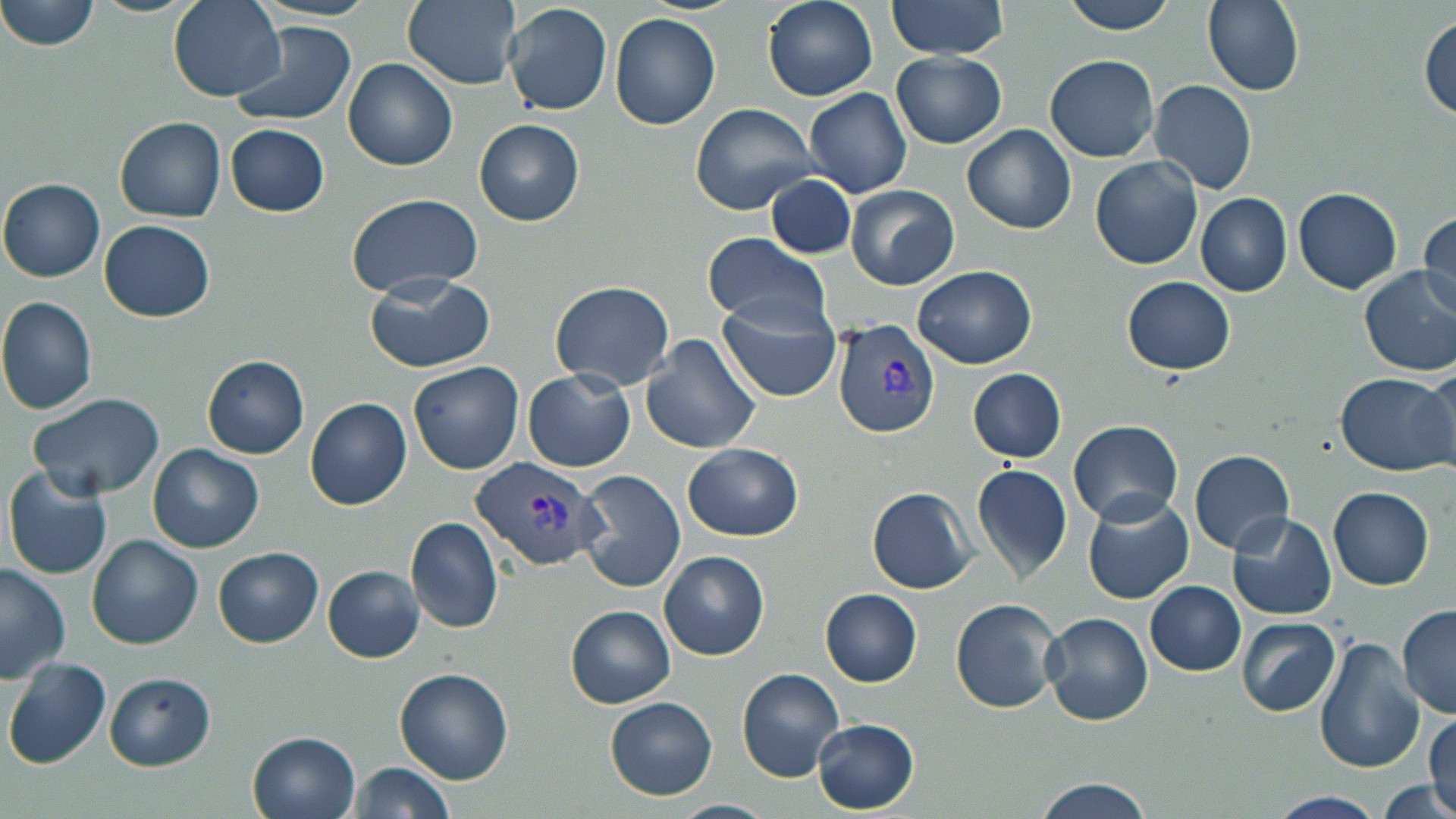

Approximate bounding boxes as named x1/y1/x2/y2 corners in pixels. Plasmodium vivax-infected red blood cell locations: (x1=833, y1=320, x2=939, y2=437), (x1=469, y1=454, x2=606, y2=572). Uninfected red blood cell locations: (x1=3, y1=0, x2=103, y2=50), (x1=169, y1=0, x2=285, y2=100), (x1=403, y1=0, x2=520, y2=89), (x1=763, y1=0, x2=879, y2=101), (x1=885, y1=0, x2=1014, y2=59), (x1=1058, y1=0, x2=1180, y2=34), (x1=1203, y1=0, x2=1304, y2=95), (x1=503, y1=1, x2=612, y2=115), (x1=610, y1=13, x2=722, y2=129), (x1=1419, y1=16, x2=1455, y2=121), (x1=229, y1=22, x2=358, y2=126), (x1=891, y1=51, x2=1008, y2=147), (x1=1045, y1=53, x2=1160, y2=161), (x1=343, y1=58, x2=457, y2=170), (x1=1150, y1=79, x2=1258, y2=195), (x1=805, y1=87, x2=912, y2=199), (x1=691, y1=101, x2=819, y2=215), (x1=115, y1=116, x2=225, y2=222), (x1=475, y1=119, x2=584, y2=225), (x1=226, y1=124, x2=329, y2=216), (x1=962, y1=125, x2=1076, y2=233), (x1=1090, y1=157, x2=1203, y2=269), (x1=766, y1=172, x2=858, y2=260), (x1=1, y1=179, x2=105, y2=281), (x1=844, y1=185, x2=959, y2=290), (x1=1294, y1=186, x2=1402, y2=294), (x1=346, y1=192, x2=482, y2=298), (x1=1195, y1=193, x2=1292, y2=295), (x1=1417, y1=212, x2=1455, y2=316), (x1=98, y1=220, x2=214, y2=322), (x1=702, y1=232, x2=833, y2=332), (x1=913, y1=265, x2=1039, y2=368), (x1=1358, y1=266, x2=1456, y2=376), (x1=364, y1=274, x2=494, y2=372), (x1=1122, y1=276, x2=1236, y2=375), (x1=550, y1=280, x2=675, y2=391), (x1=717, y1=296, x2=843, y2=404), (x1=0, y1=297, x2=97, y2=414), (x1=643, y1=335, x2=762, y2=457), (x1=202, y1=356, x2=310, y2=458), (x1=409, y1=361, x2=524, y2=474), (x1=1422, y1=363, x2=1456, y2=467), (x1=969, y1=368, x2=1067, y2=463), (x1=524, y1=370, x2=635, y2=472), (x1=1337, y1=372, x2=1456, y2=474), (x1=29, y1=393, x2=166, y2=499), (x1=306, y1=398, x2=412, y2=510), (x1=1068, y1=419, x2=1183, y2=526), (x1=682, y1=441, x2=802, y2=540), (x1=150, y1=443, x2=263, y2=553), (x1=1189, y1=448, x2=1294, y2=554), (x1=971, y1=462, x2=1073, y2=582), (x1=5, y1=466, x2=113, y2=579), (x1=577, y1=469, x2=686, y2=592), (x1=867, y1=487, x2=977, y2=595), (x1=1329, y1=487, x2=1434, y2=589), (x1=1083, y1=492, x2=1192, y2=604), (x1=1228, y1=511, x2=1336, y2=621), (x1=407, y1=517, x2=503, y2=634), (x1=87, y1=534, x2=206, y2=650), (x1=213, y1=547, x2=323, y2=647), (x1=660, y1=550, x2=769, y2=660), (x1=0, y1=561, x2=72, y2=682), (x1=322, y1=565, x2=425, y2=662), (x1=1145, y1=582, x2=1245, y2=675), (x1=820, y1=588, x2=923, y2=686), (x1=951, y1=598, x2=1062, y2=712), (x1=1398, y1=603, x2=1456, y2=717), (x1=566, y1=605, x2=675, y2=708), (x1=1042, y1=611, x2=1154, y2=725), (x1=1236, y1=617, x2=1342, y2=716), (x1=1314, y1=637, x2=1423, y2=773), (x1=5, y1=657, x2=111, y2=770), (x1=394, y1=667, x2=514, y2=785), (x1=737, y1=667, x2=843, y2=781), (x1=104, y1=673, x2=215, y2=769), (x1=606, y1=697, x2=716, y2=799), (x1=1428, y1=708, x2=1456, y2=814), (x1=813, y1=719, x2=919, y2=813), (x1=248, y1=731, x2=361, y2=819), (x1=346, y1=761, x2=458, y2=819), (x1=1030, y1=778, x2=1155, y2=818), (x1=1378, y1=778, x2=1452, y2=819), (x1=1268, y1=792, x2=1385, y2=819), (x1=667, y1=800, x2=776, y2=819). Slide-level diagnosis: Plasmodium vivax. Optical microscopy. Image is 1456×819 pixels. One field of a larger specimen. Thin blood smear. May-Grünwald-Giemsa-stained preparation. Captured at 1000x magnification.